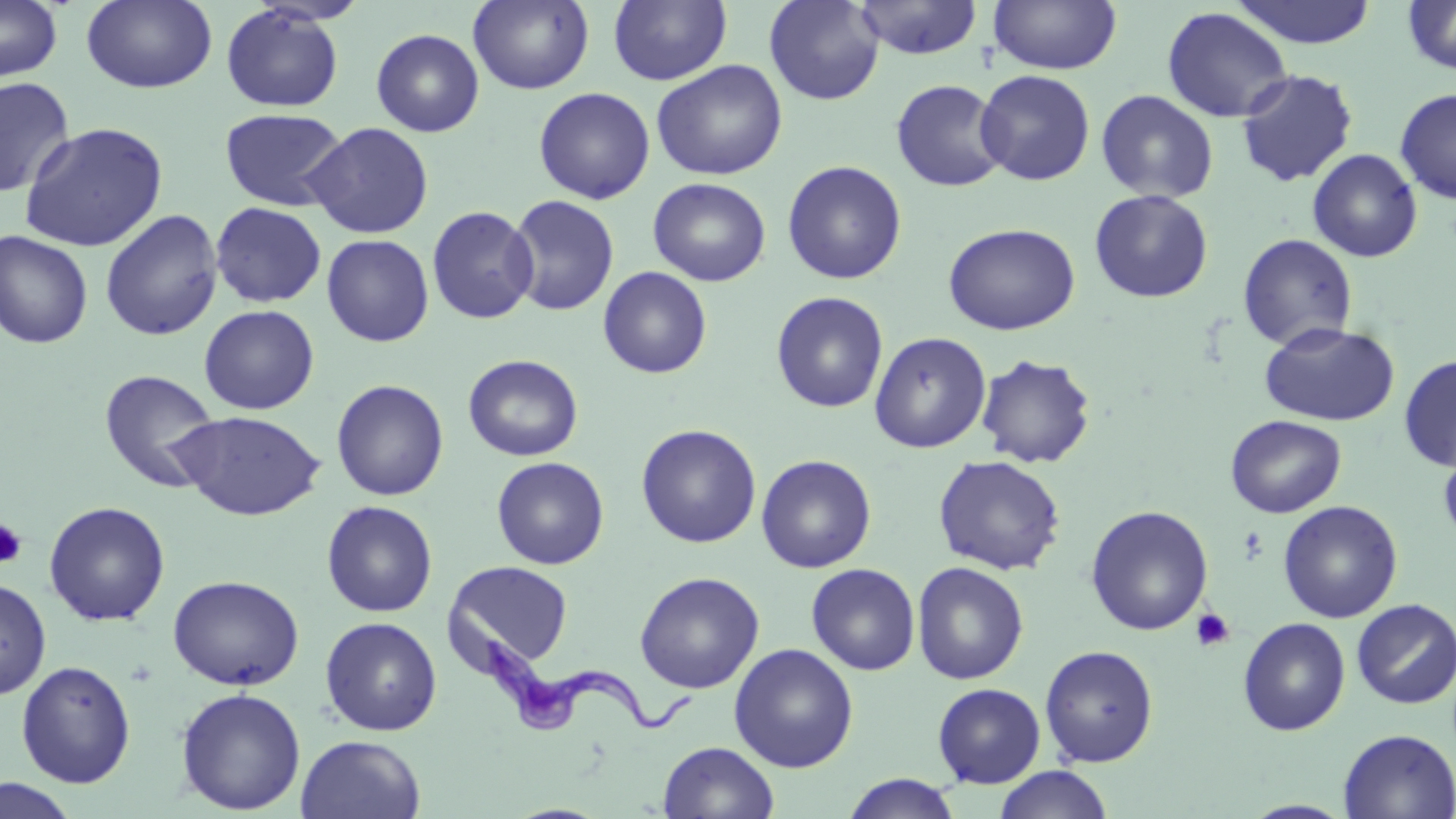
Summary:
  - Coordinate format: approximate bounding boxes as [x1, y1, x2, y2] in pixels
  - Platelet locations: [0, 517, 27, 568], [1190, 608, 1235, 653]
  - Uninfected red blood cell locations: [0, 0, 62, 83], [81, 0, 217, 94], [468, 0, 594, 94], [608, 0, 732, 86], [764, 0, 885, 105], [852, 0, 983, 58], [988, 0, 1122, 74], [1230, 0, 1378, 48], [1402, 0, 1456, 75], [221, 5, 344, 112], [1162, 7, 1293, 123], [371, 28, 485, 137], [651, 59, 788, 180], [975, 69, 1095, 186], [1236, 69, 1358, 187], [0, 77, 75, 198], [890, 79, 1009, 192], [533, 87, 655, 204], [1395, 88, 1456, 204], [1095, 89, 1219, 203], [219, 107, 349, 211], [303, 121, 434, 238], [18, 122, 169, 252], [1307, 148, 1422, 263], [781, 160, 907, 284], [647, 177, 771, 286], [1089, 189, 1213, 303], [504, 195, 619, 316], [210, 202, 326, 307], [426, 205, 539, 324], [99, 209, 223, 342], [944, 222, 1080, 335], [0, 230, 94, 349], [1237, 233, 1358, 351], [321, 234, 434, 347], [597, 266, 712, 379], [770, 292, 889, 413], [199, 304, 320, 415], [1259, 321, 1400, 427], [869, 332, 992, 453], [975, 353, 1096, 468], [463, 354, 583, 461], [1398, 354, 1456, 471], [99, 368, 222, 494], [331, 379, 449, 501], [174, 410, 325, 521], [1225, 415, 1346, 517], [636, 424, 762, 548], [1438, 438, 1456, 551], [635, 442, 875, 559], [756, 454, 876, 573], [933, 454, 1066, 575], [491, 456, 609, 569], [44, 500, 170, 626], [321, 500, 437, 617], [1278, 500, 1403, 623], [1085, 505, 1213, 635], [446, 560, 573, 670], [911, 561, 1029, 685], [806, 563, 920, 675], [634, 571, 765, 693], [167, 575, 305, 690], [0, 576, 51, 700], [1351, 598, 1456, 709], [320, 616, 442, 736], [1238, 617, 1351, 735], [729, 643, 859, 773], [1039, 644, 1159, 766], [16, 660, 137, 787], [932, 683, 1046, 787], [175, 687, 306, 814], [1338, 729, 1456, 818], [295, 734, 427, 819], [658, 741, 779, 819], [993, 765, 1114, 818], [841, 773, 963, 818], [0, 775, 81, 818], [1241, 800, 1356, 818]
  - Trypanosoma brucei locations: [475, 626, 698, 737]
  - Slide-level diagnosis: Trypanosoma brucei
  - Field of view: single
  - Image size: 1456×819 pixels
  - Stain: May-Grünwald-Giemsa
  - Preparation: thin blood film
  - Modality: light microscopy
  - Magnification: 1000x